Identify the parasite.
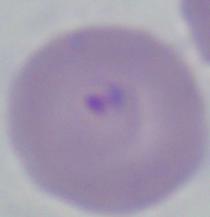
This is Babesia.

modality = micrograph
magnification = 1000x